Locate every uninfected red blood cell.
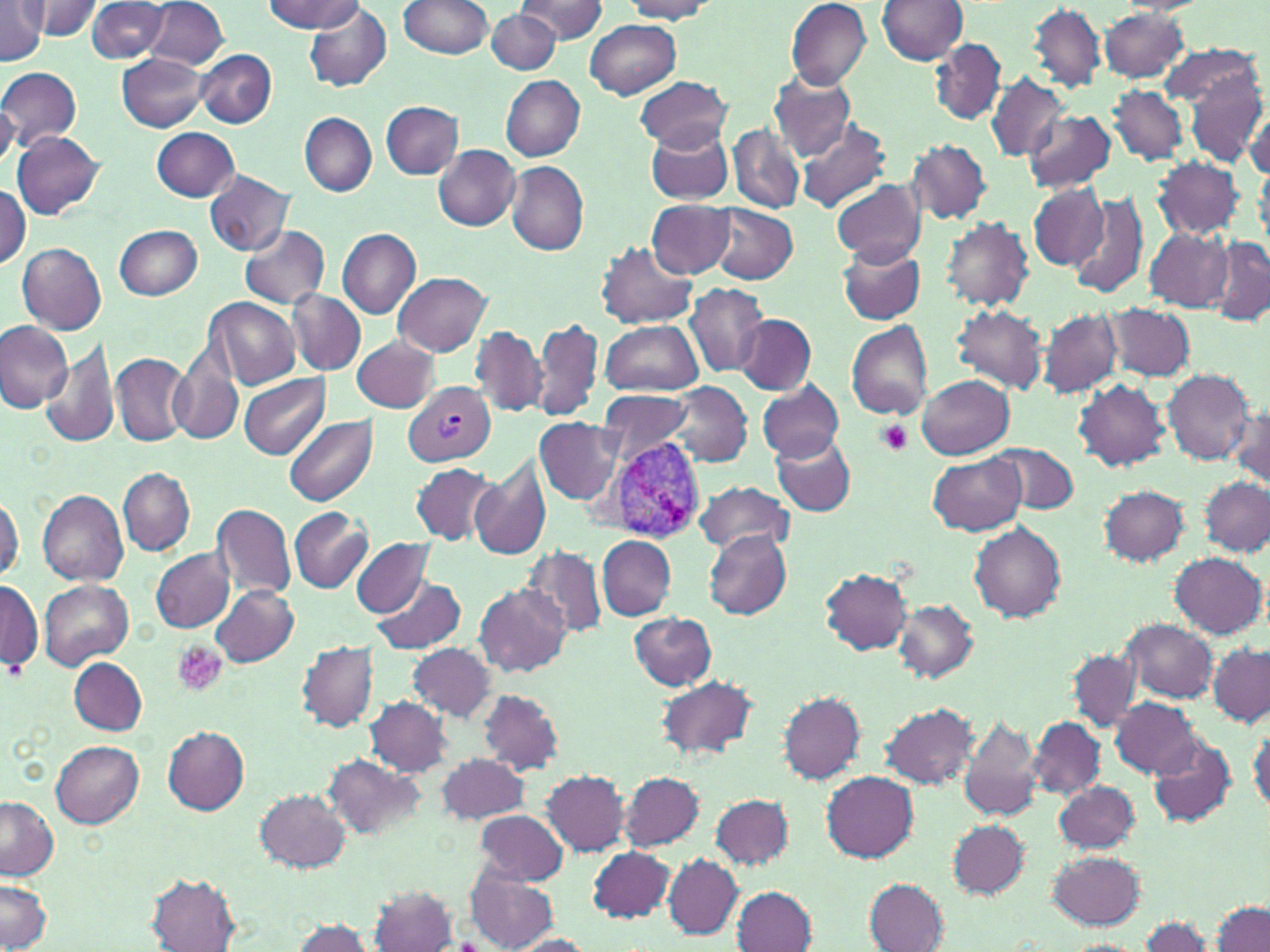
Approximate bounding boxes as (x1,y1)-(x2,y2) corner pairs in pixels.
Uninfected red blood cells: (0,0)-(48,64), (31,0)-(103,40), (263,0)-(364,33), (399,0)-(494,59), (519,0)-(608,43), (786,0)-(871,90), (877,0)-(968,65), (145,1)-(229,71), (622,1)-(712,21), (84,2)-(170,62), (1028,3)-(1105,92), (303,4)-(392,91), (1099,8)-(1189,83), (486,9)-(560,75), (583,19)-(680,100), (931,39)-(1005,124), (1158,43)-(1261,114), (194,48)-(277,128), (118,52)-(210,132), (1180,55)-(1267,168), (0,67)-(82,151), (769,72)-(855,159), (985,74)-(1069,162), (500,75)-(585,161), (636,76)-(731,151), (1108,85)-(1188,167), (381,100)-(463,178), (1246,105)-(1270,180), (1023,110)-(1115,194), (301,114)-(376,196), (795,118)-(893,215), (728,124)-(804,213), (645,126)-(734,204), (151,127)-(240,201), (11,131)-(104,218), (907,139)-(992,226), (433,144)-(520,231), (1152,158)-(1245,239), (506,162)-(588,256), (204,172)-(293,256), (832,178)-(925,267), (1028,184)-(1107,269), (0,186)-(30,272), (1067,191)-(1151,301), (646,199)-(734,279), (706,204)-(798,284), (939,215)-(1035,311), (114,224)-(202,299), (240,224)-(329,308), (1144,226)-(1233,312), (336,228)-(421,318), (1207,237)-(1270,327), (596,241)-(698,329), (17,243)-(106,334), (837,244)-(925,325), (392,272)-(491,356), (684,281)-(767,377), (287,290)-(365,374), (203,297)-(301,390), (1104,302)-(1195,383), (950,304)-(1047,394), (1038,308)-(1123,398), (734,314)-(817,394), (531,316)-(603,422), (601,320)-(702,395), (845,320)-(935,420), (0,321)-(72,414), (471,326)-(548,417), (351,335)-(439,411), (41,338)-(120,450), (170,349)-(243,446), (111,354)-(192,446), (1161,369)-(1256,465), (239,373)-(331,458), (916,375)-(1014,459), (756,378)-(845,462), (664,380)-(752,468), (1074,381)-(1170,471), (598,390)-(694,464), (1231,400)-(1270,490), (284,416)-(377,506), (535,419)-(622,504), (773,435)-(856,516), (990,442)-(1078,512), (927,453)-(1027,536), (470,456)-(552,562), (412,462)-(499,544), (118,467)-(195,555), (1201,477)-(1269,557), (694,481)-(794,556), (1099,485)-(1190,566), (38,489)-(129,585), (1,496)-(23,581), (212,502)-(296,600), (289,506)-(369,594), (968,522)-(1067,622), (704,530)-(791,618), (597,536)-(676,620), (351,538)-(433,617), (522,546)-(608,639), (151,549)-(234,633), (1170,553)-(1266,639), (819,567)-(913,654), (369,575)-(468,655), (0,578)-(42,677), (38,578)-(133,669), (210,585)-(299,666), (474,585)-(570,677), (894,599)-(978,682), (628,612)-(716,691), (1119,619)-(1215,704), (297,641)-(378,731), (407,643)-(497,721), (1208,645)-(1270,726), (1069,650)-(1139,733), (70,658)-(147,734), (656,675)-(759,761), (478,689)-(564,773), (779,691)-(866,784), (364,697)-(452,776), (1110,698)-(1199,779), (879,703)-(979,789), (958,716)-(1042,821), (1028,718)-(1104,801), (1248,720)-(1269,818), (161,727)-(250,815), (1147,734)-(1236,830), (51,741)-(145,828), (435,753)-(530,824), (323,755)-(424,842), (543,771)-(629,855), (821,771)-(919,862), (620,772)-(704,850), (1054,782)-(1140,852), (255,789)-(350,873), (709,793)-(794,870), (0,796)-(59,879), (473,809)-(569,884), (947,821)-(1028,898), (587,846)-(675,921), (1047,851)-(1146,930), (662,854)-(743,939), (466,867)-(558,952), (146,874)-(240,951), (1,879)-(53,952), (865,879)-(948,952), (370,885)-(456,952), (733,886)-(817,951), (1212,901)-(1270,952), (1136,916)-(1212,952), (289,917)-(373,952), (509,934)-(594,951).

slide-level diagnosis = Plasmodium vivax
platelet locations = approximate bounding boxes as (x1,y1)-(x2,y2) corner pairs in pixels: (877,420)-(912,455), (174,642)-(229,697)
field of view = single
stain = May-Grünwald-Giemsa
preparation = thin blood smear
Plasmodium vivax-infected red blood cell locations = approximate bounding boxes as (x1,y1)-(x2,y2) corner pairs in pixels: (405,383)-(496,464), (602,436)-(708,540)
modality = optical microscopy
image size = 1270×952 pixels
magnification = 1000x